Describe the morphology of the erythrocytes.
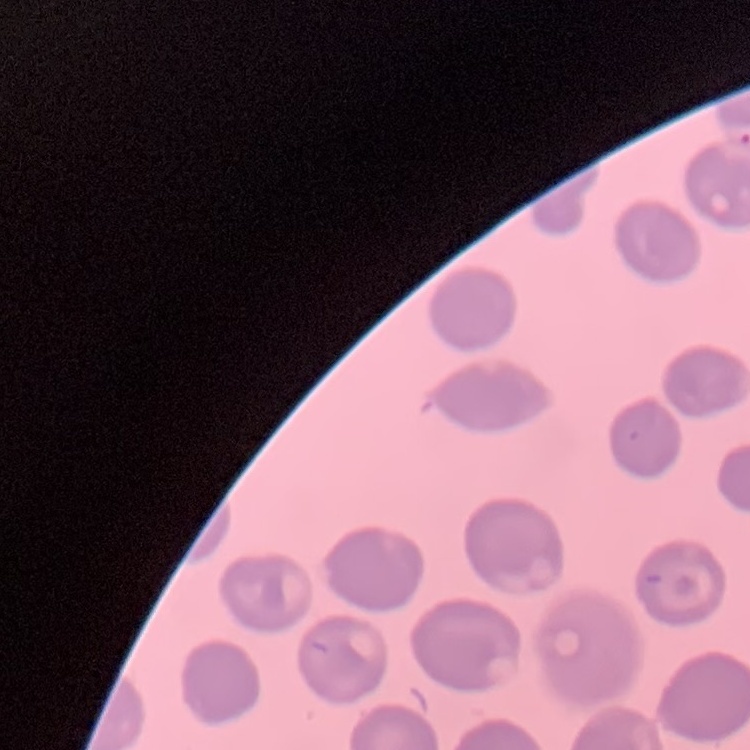

No rouleaux formation.

{
  "stain": "Field's or Giemsa",
  "image_type": "square crop of a larger photomicrograph",
  "preparation": "thin blood smear"
}